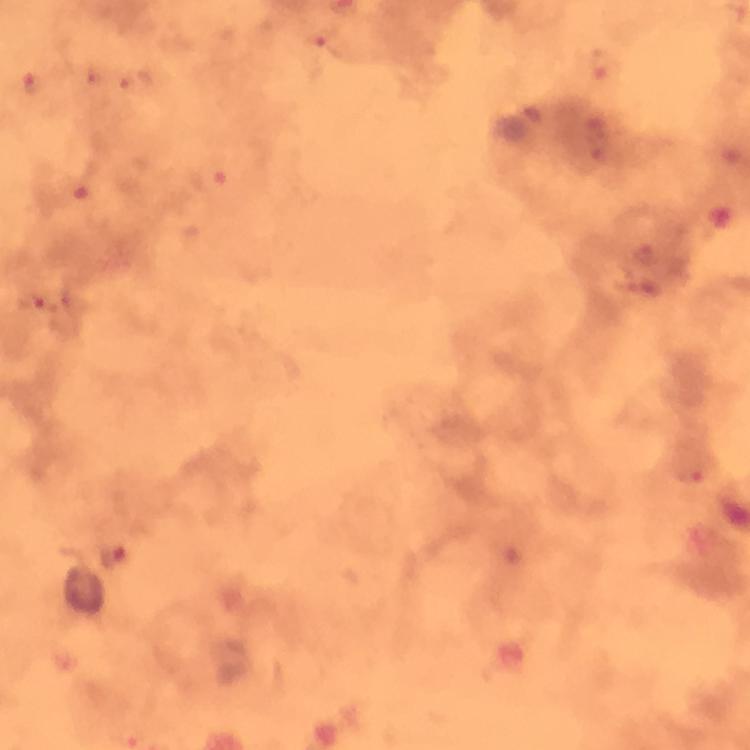

cropped from = one field of view
context = from a diagnostic examination for malaria
magnification = 100x
Plasmodium parasite locations = approximate centers as (x, y) in pixels: (326, 42), (602, 70), (135, 80), (33, 83), (596, 138), (209, 176), (80, 187), (647, 255), (33, 301), (693, 476), (112, 555), (131, 737)
image size = 750×750 pixels
capture = smartphone mounted on the microscope
immersion oil = used
preparation = thick smear
stain = Giemsa